Classify this cell by malaria status.
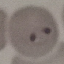

It is parasitized.

image type = automatically extracted cell patch, resized to 64 × 64 pixels
capture = smartphone through the microscope eyepiece
stain = Giemsa
preparation = thin blood film